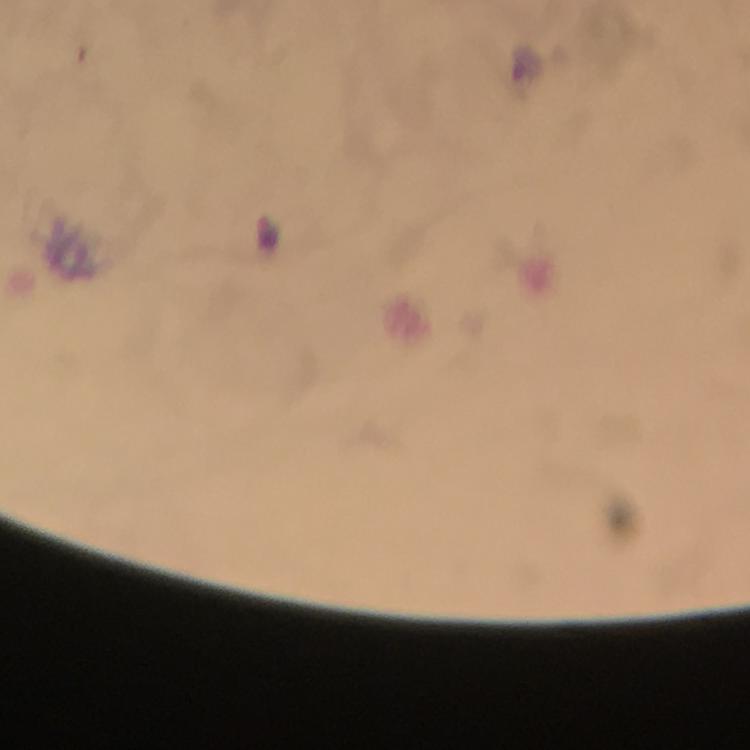

Approximate object centers, in pixels from the top-left corner.
Summary:
  - Plasmodium parasite locations: (x=526, y=64), (x=266, y=232)
  - Preparation: thick blood smear
  - Cropped from: one field of view
  - Magnification: 100x
  - Image size: 750×750 pixels
  - Stain: Giemsa
  - Capture: smartphone camera through the microscope
  - Immersion oil: used
  - Context: from a malaria diagnostic workup